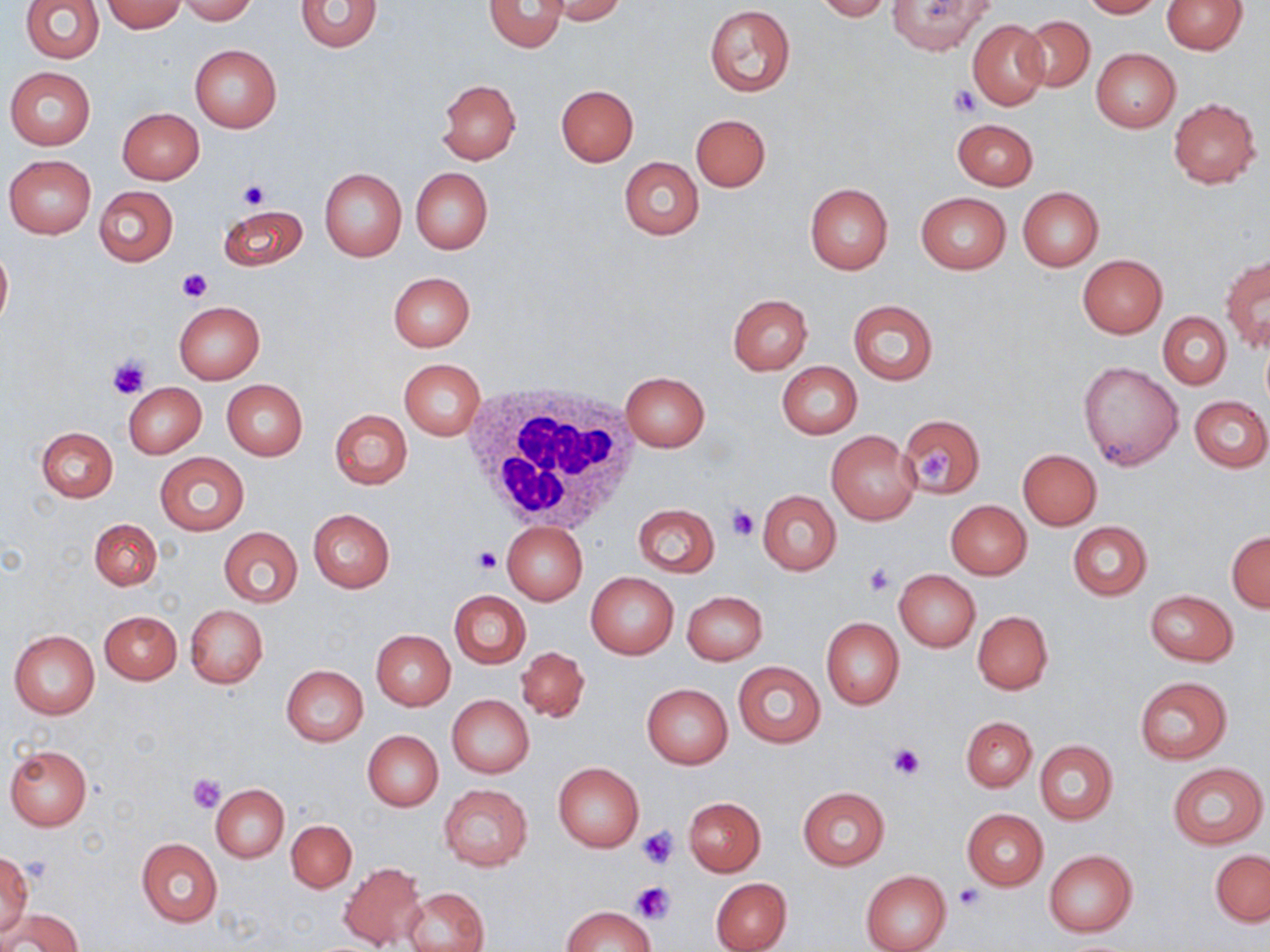

Summary:
  - Coordinate format: approximate bounding boxes as named x1/y1/x2/y2 corners in pixels
  - Uninfected red blood cell locations: (x1=19, y1=0, x2=105, y2=63), (x1=177, y1=0, x2=258, y2=24), (x1=294, y1=0, x2=383, y2=52), (x1=538, y1=0, x2=628, y2=25), (x1=813, y1=0, x2=892, y2=21), (x1=1081, y1=0, x2=1161, y2=18), (x1=1161, y1=0, x2=1245, y2=54), (x1=101, y1=1, x2=186, y2=32), (x1=481, y1=1, x2=568, y2=53), (x1=887, y1=1, x2=995, y2=54), (x1=703, y1=5, x2=795, y2=97), (x1=1019, y1=15, x2=1094, y2=92), (x1=967, y1=19, x2=1049, y2=111), (x1=189, y1=45, x2=281, y2=133), (x1=1090, y1=47, x2=1181, y2=133), (x1=5, y1=67, x2=96, y2=150), (x1=437, y1=80, x2=521, y2=165), (x1=556, y1=85, x2=638, y2=166), (x1=1167, y1=99, x2=1262, y2=188), (x1=117, y1=108, x2=204, y2=184), (x1=691, y1=114, x2=770, y2=192), (x1=952, y1=118, x2=1037, y2=189), (x1=3, y1=155, x2=96, y2=238), (x1=619, y1=156, x2=704, y2=240), (x1=411, y1=167, x2=492, y2=254), (x1=319, y1=168, x2=407, y2=262), (x1=804, y1=182, x2=893, y2=273), (x1=94, y1=185, x2=178, y2=265), (x1=1017, y1=187, x2=1104, y2=269), (x1=915, y1=192, x2=1011, y2=274), (x1=216, y1=204, x2=307, y2=272), (x1=0, y1=241, x2=12, y2=331), (x1=1221, y1=253, x2=1269, y2=350), (x1=1077, y1=254, x2=1168, y2=338), (x1=387, y1=271, x2=475, y2=352), (x1=727, y1=294, x2=812, y2=375), (x1=847, y1=299, x2=938, y2=384), (x1=173, y1=302, x2=265, y2=383), (x1=1158, y1=313, x2=1231, y2=388), (x1=400, y1=360, x2=485, y2=440), (x1=777, y1=362, x2=862, y2=439), (x1=1079, y1=362, x2=1183, y2=470), (x1=620, y1=371, x2=709, y2=451), (x1=221, y1=379, x2=308, y2=459), (x1=123, y1=381, x2=206, y2=458), (x1=1189, y1=395, x2=1270, y2=473), (x1=329, y1=409, x2=412, y2=489), (x1=898, y1=415, x2=985, y2=498), (x1=36, y1=427, x2=117, y2=502), (x1=826, y1=430, x2=919, y2=523), (x1=1018, y1=449, x2=1102, y2=529), (x1=155, y1=453, x2=249, y2=536), (x1=756, y1=490, x2=842, y2=575), (x1=945, y1=500, x2=1031, y2=580), (x1=632, y1=504, x2=719, y2=578), (x1=308, y1=509, x2=395, y2=593), (x1=90, y1=518, x2=161, y2=590), (x1=501, y1=521, x2=587, y2=605), (x1=1067, y1=522, x2=1152, y2=600), (x1=218, y1=527, x2=302, y2=607), (x1=1226, y1=531, x2=1270, y2=612), (x1=894, y1=569, x2=981, y2=652), (x1=586, y1=572, x2=678, y2=659), (x1=1145, y1=589, x2=1239, y2=666), (x1=449, y1=590, x2=530, y2=668), (x1=681, y1=590, x2=768, y2=665), (x1=185, y1=604, x2=268, y2=688), (x1=100, y1=610, x2=181, y2=684), (x1=973, y1=611, x2=1052, y2=694), (x1=821, y1=618, x2=904, y2=709), (x1=9, y1=628, x2=100, y2=719), (x1=371, y1=629, x2=455, y2=710), (x1=516, y1=646, x2=589, y2=722), (x1=733, y1=661, x2=825, y2=748), (x1=281, y1=664, x2=368, y2=746), (x1=1133, y1=676, x2=1232, y2=764), (x1=642, y1=683, x2=732, y2=769), (x1=447, y1=694, x2=534, y2=778), (x1=961, y1=716, x2=1036, y2=791), (x1=362, y1=730, x2=443, y2=811), (x1=1034, y1=741, x2=1118, y2=825), (x1=4, y1=746, x2=91, y2=831), (x1=553, y1=761, x2=644, y2=852), (x1=1167, y1=763, x2=1267, y2=848), (x1=210, y1=783, x2=289, y2=862), (x1=438, y1=784, x2=532, y2=870), (x1=797, y1=787, x2=889, y2=869), (x1=684, y1=797, x2=765, y2=876), (x1=961, y1=808, x2=1048, y2=890), (x1=287, y1=819, x2=356, y2=892), (x1=136, y1=838, x2=222, y2=927), (x1=1044, y1=850, x2=1137, y2=936), (x1=1210, y1=850, x2=1269, y2=926), (x1=0, y1=851, x2=33, y2=942), (x1=339, y1=862, x2=427, y2=950), (x1=860, y1=870, x2=951, y2=952), (x1=710, y1=877, x2=792, y2=952), (x1=404, y1=888, x2=488, y2=952), (x1=562, y1=906, x2=654, y2=952), (x1=5, y1=908, x2=81, y2=952)
  - White blood cell locations: (x1=460, y1=385, x2=638, y2=533)
  - Platelet locations: (x1=949, y1=84, x2=982, y2=116), (x1=237, y1=178, x2=270, y2=208), (x1=179, y1=269, x2=211, y2=302), (x1=106, y1=354, x2=150, y2=399), (x1=917, y1=446, x2=954, y2=484), (x1=728, y1=504, x2=759, y2=541), (x1=473, y1=547, x2=504, y2=575), (x1=864, y1=564, x2=894, y2=596), (x1=888, y1=742, x2=924, y2=778), (x1=189, y1=772, x2=226, y2=812), (x1=638, y1=827, x2=679, y2=867), (x1=26, y1=855, x2=49, y2=885), (x1=630, y1=881, x2=677, y2=921), (x1=954, y1=885, x2=983, y2=910)
  - Slide-level diagnosis: no evidence of blood parasites
  - Magnification: 1000x
  - Preparation: thin blood smear
  - Stain: May-Grünwald-Giemsa
  - Image size: 1270×952 pixels
  - Field of view: single
  - Modality: light microscopy